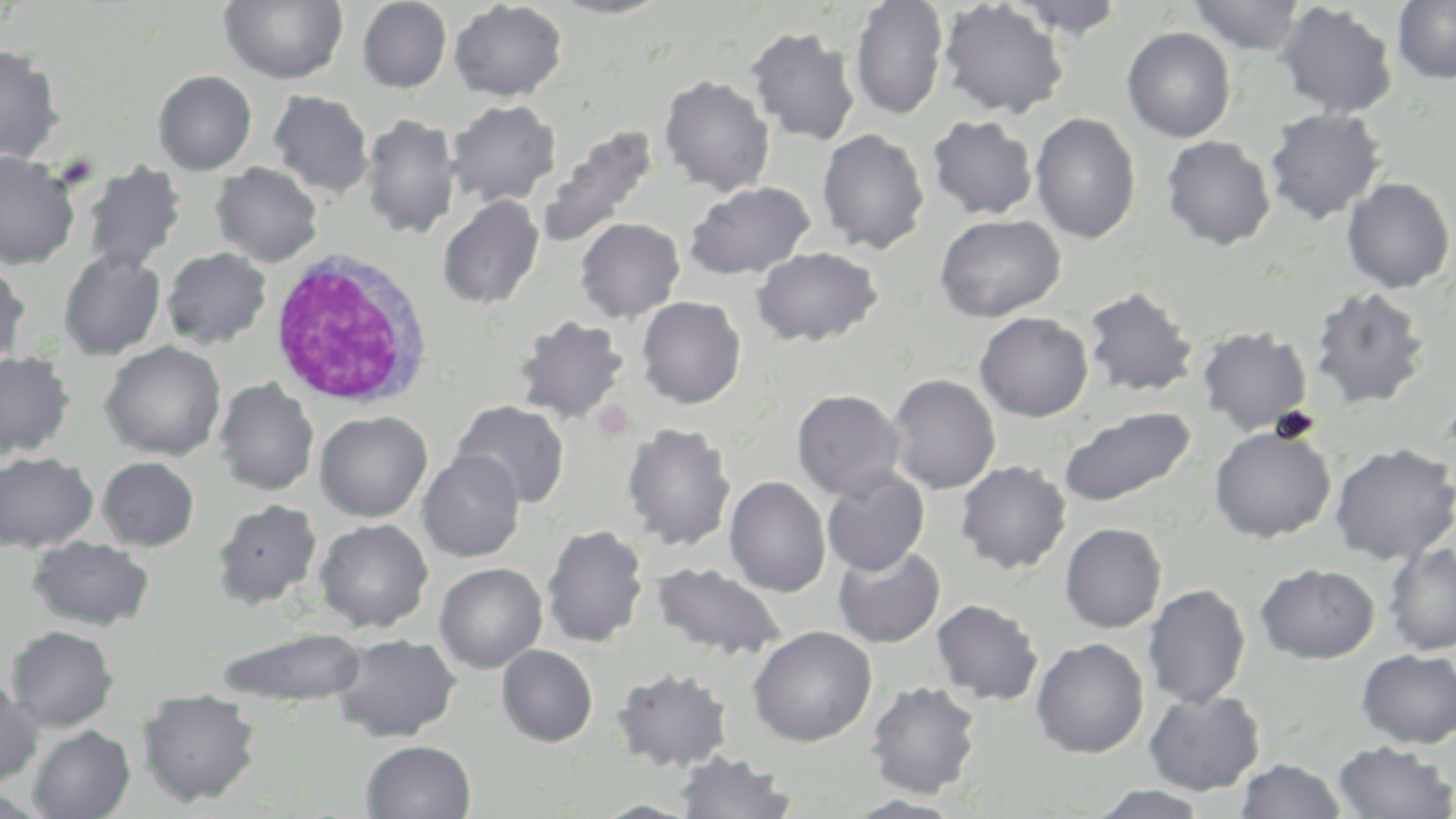

Summary:
  - Coordinate format: approximate bounding boxes as (x1, y1, x2, y2) in pixels
  - Platelet locations: (52, 152, 100, 191)
  - Uninfected red blood cell locations: (219, 0, 348, 84), (544, 0, 674, 19), (850, 0, 949, 119), (939, 0, 1069, 118), (1187, 0, 1306, 56), (1392, 0, 1456, 84), (357, 1, 452, 92), (1003, 1, 1127, 38), (449, 2, 567, 101), (1275, 2, 1398, 118), (746, 26, 861, 146), (1122, 27, 1236, 142), (0, 44, 64, 165), (153, 70, 257, 174), (659, 75, 775, 196), (268, 90, 374, 197), (446, 99, 561, 207), (1264, 108, 1386, 224), (359, 111, 461, 240), (1030, 112, 1141, 243), (928, 115, 1038, 219), (537, 125, 659, 249), (817, 128, 930, 253), (1161, 135, 1275, 249), (0, 151, 80, 269), (211, 162, 323, 267), (81, 165, 186, 273), (1341, 177, 1455, 292), (684, 181, 816, 280), (438, 195, 544, 309), (935, 214, 1065, 321), (575, 217, 685, 323), (162, 247, 272, 349), (752, 247, 882, 347), (58, 249, 166, 360), (0, 261, 31, 371), (1082, 286, 1199, 398), (1309, 286, 1430, 410), (637, 296, 747, 408), (974, 312, 1093, 421), (511, 315, 629, 425), (1197, 326, 1312, 434), (100, 341, 226, 460), (0, 351, 75, 459), (887, 373, 1000, 494), (214, 378, 319, 496), (791, 389, 905, 500), (451, 400, 571, 508), (1058, 407, 1195, 507), (314, 411, 433, 522), (621, 421, 737, 550), (1209, 425, 1335, 542), (1329, 443, 1456, 564), (418, 451, 526, 561), (0, 452, 98, 552), (97, 457, 200, 551), (956, 460, 1072, 572), (822, 467, 930, 576), (724, 477, 831, 597), (210, 498, 323, 609), (315, 518, 433, 632), (1060, 522, 1167, 633), (542, 524, 649, 648), (28, 536, 154, 630), (1384, 543, 1455, 656), (833, 545, 946, 647), (434, 562, 547, 672), (652, 562, 788, 660), (1255, 563, 1379, 664), (1143, 584, 1250, 708), (931, 598, 1043, 705), (5, 625, 119, 731), (748, 625, 877, 746), (212, 627, 371, 707), (331, 633, 463, 742), (1031, 637, 1149, 758), (496, 645, 598, 746), (1356, 649, 1456, 747), (612, 668, 732, 771), (0, 679, 43, 787), (866, 681, 981, 798), (138, 689, 261, 806), (1143, 689, 1265, 795), (28, 725, 135, 818), (361, 740, 476, 819), (1332, 741, 1455, 818), (672, 752, 798, 818), (1235, 758, 1346, 818), (1089, 785, 1212, 819), (846, 795, 965, 817), (588, 798, 704, 818)
  - White blood cell locations: (270, 248, 435, 409)
  - Slide-level diagnosis: negative for blood parasites
  - Image size: 1456×819 pixels
  - Stain: May-Grünwald-Giemsa
  - Modality: optical microscopy
  - Magnification: 1000x
  - Preparation: thin blood film
  - Field of view: single